State the preparation type.
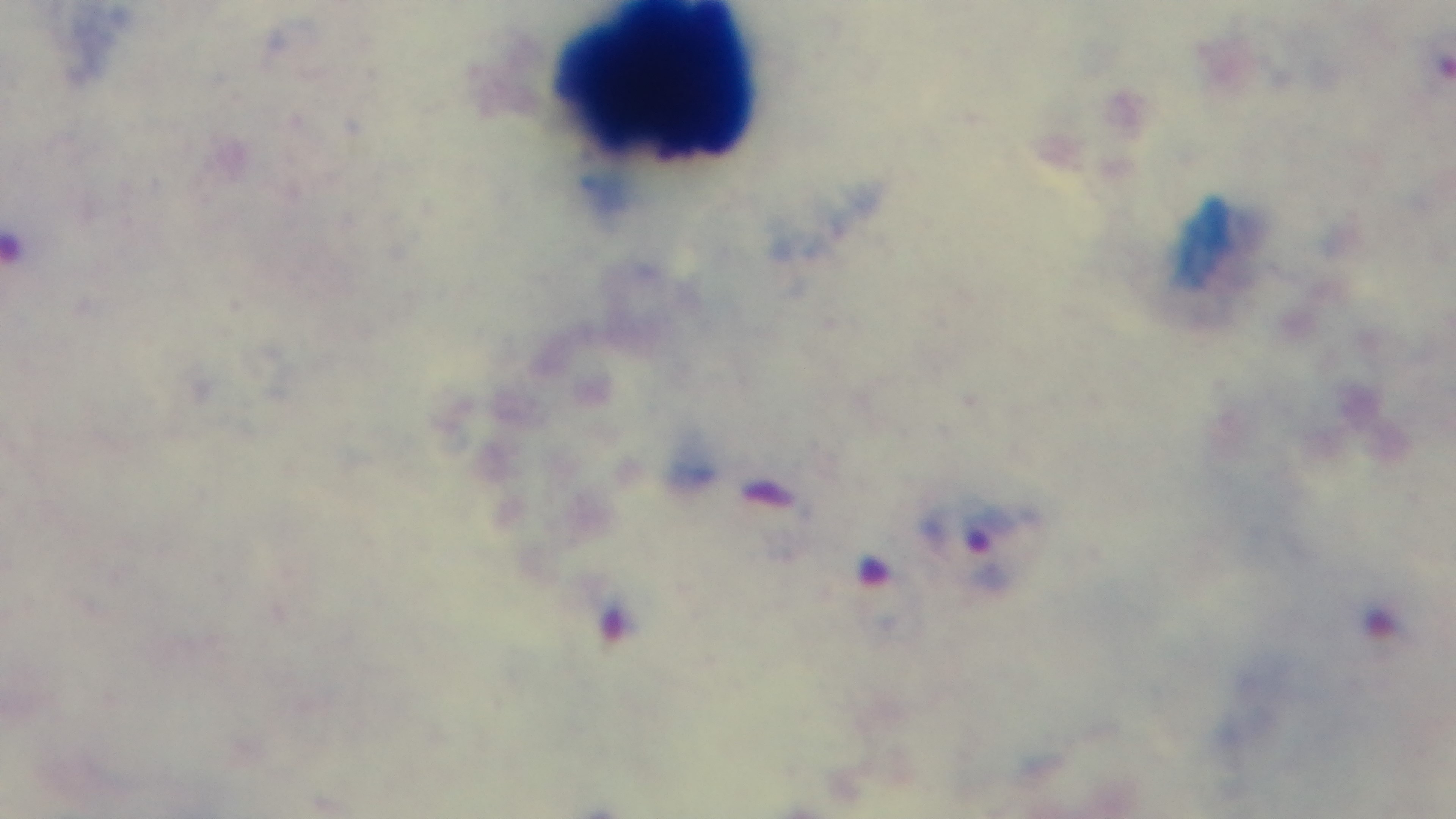

A thick smear.

Malaria status: infected. Single field of view. Giemsa stain. Captured with a mounted 4K digital camera. Oil-immersion objective, 100x. Light microscopy.